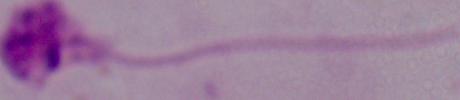
Captured at 1000x magnification. Micrograph. A Leishmania parasite is seen.